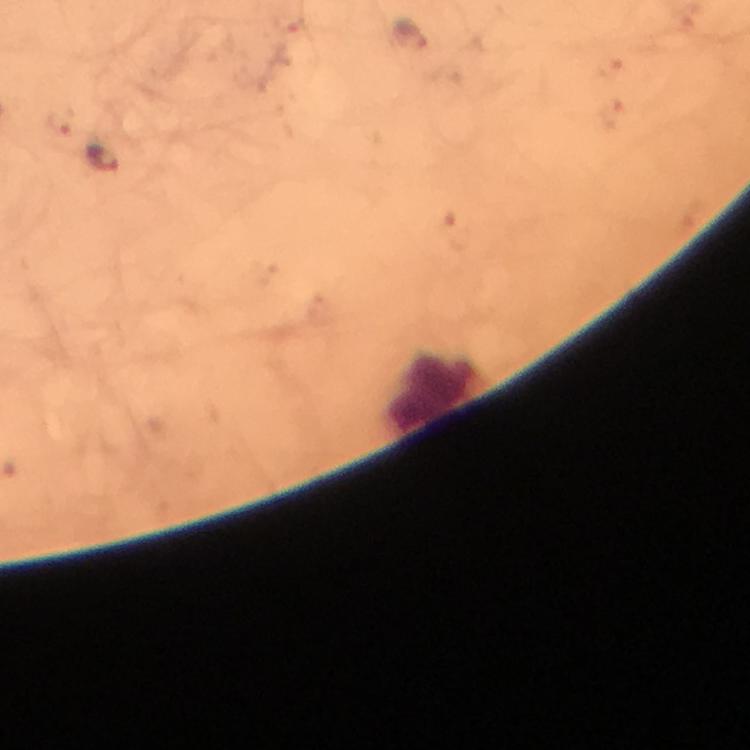

Approximate centers as {x, y} in pixels. Malaria parasite locations: {103, 157}. Leukocyte locations: {433, 392}. A crop from one field of view. Immersion oil applied. Image is 750×750 pixels. Giemsa-stained preparation. Photographed with a smartphone mounted on the microscope. From a diagnostic examination for malaria. Thick blood smear. 100x magnification.